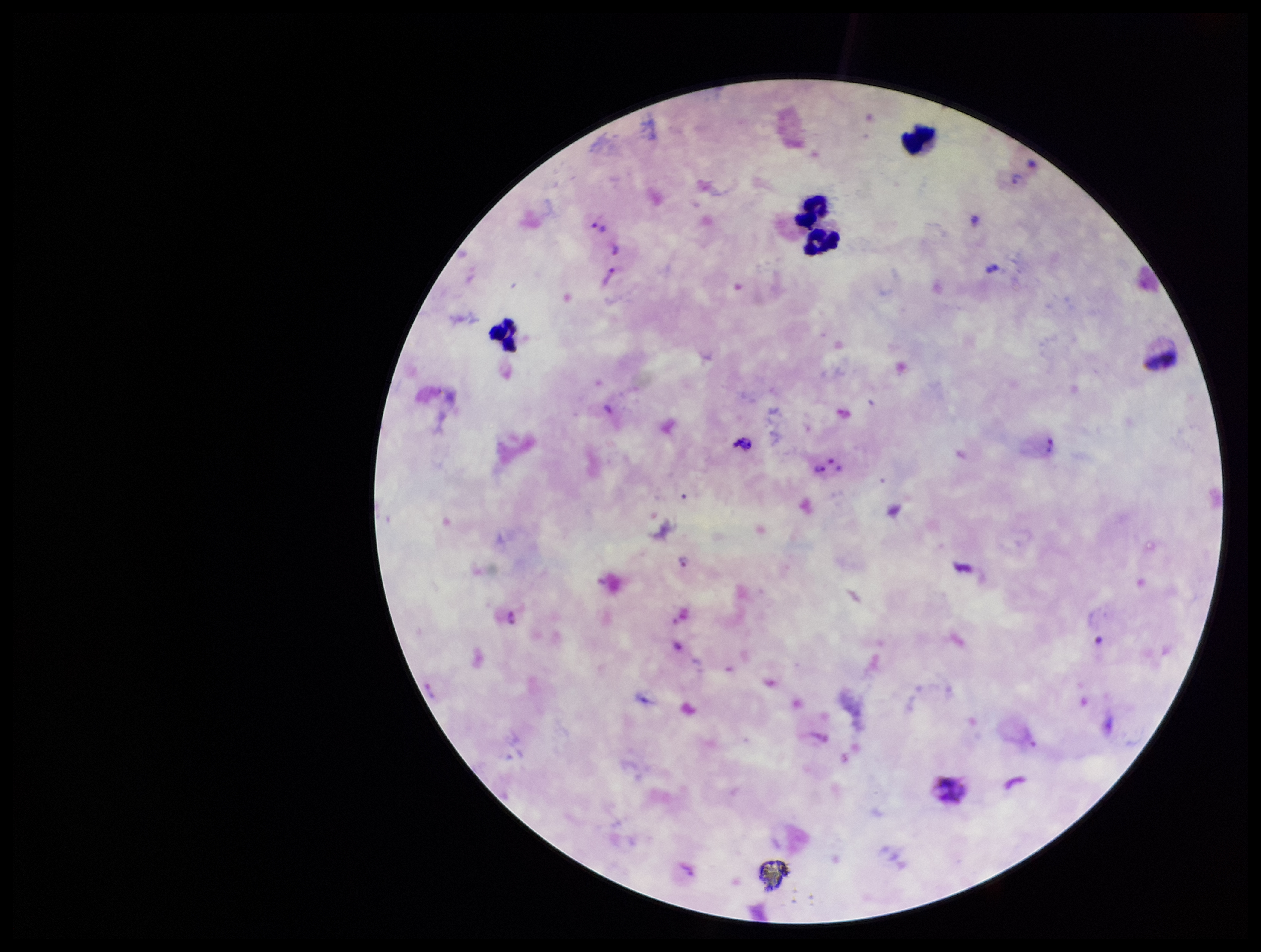
Summary:
  - Parasite count: 10
  - Field of view: single
  - Stain: Giemsa
  - Plasmodium parasites: seen
  - Patient malaria status: infected
  - Capture: smartphone photograph through the microscope eyepiece
  - Preparation: thick
  - Leukocyte count: 4
  - Species reported for this patient: Plasmodium vivax
  - Image size: 1261×952 pixels